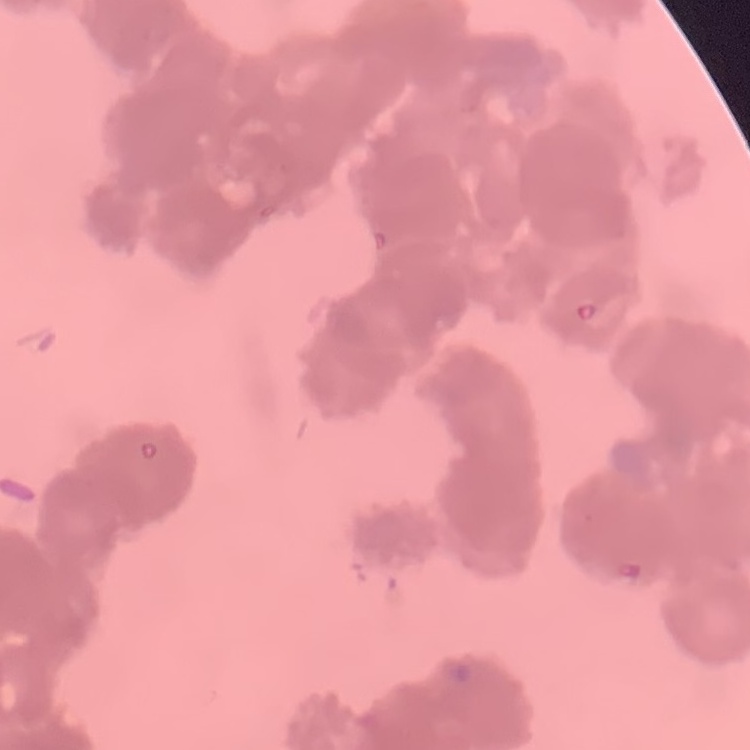

red_blood_cell_morphology: rouleaux formation
image_type: one tile cut from a larger photomicrograph
preparation: thin blood smear
stain: Field's or Giemsa